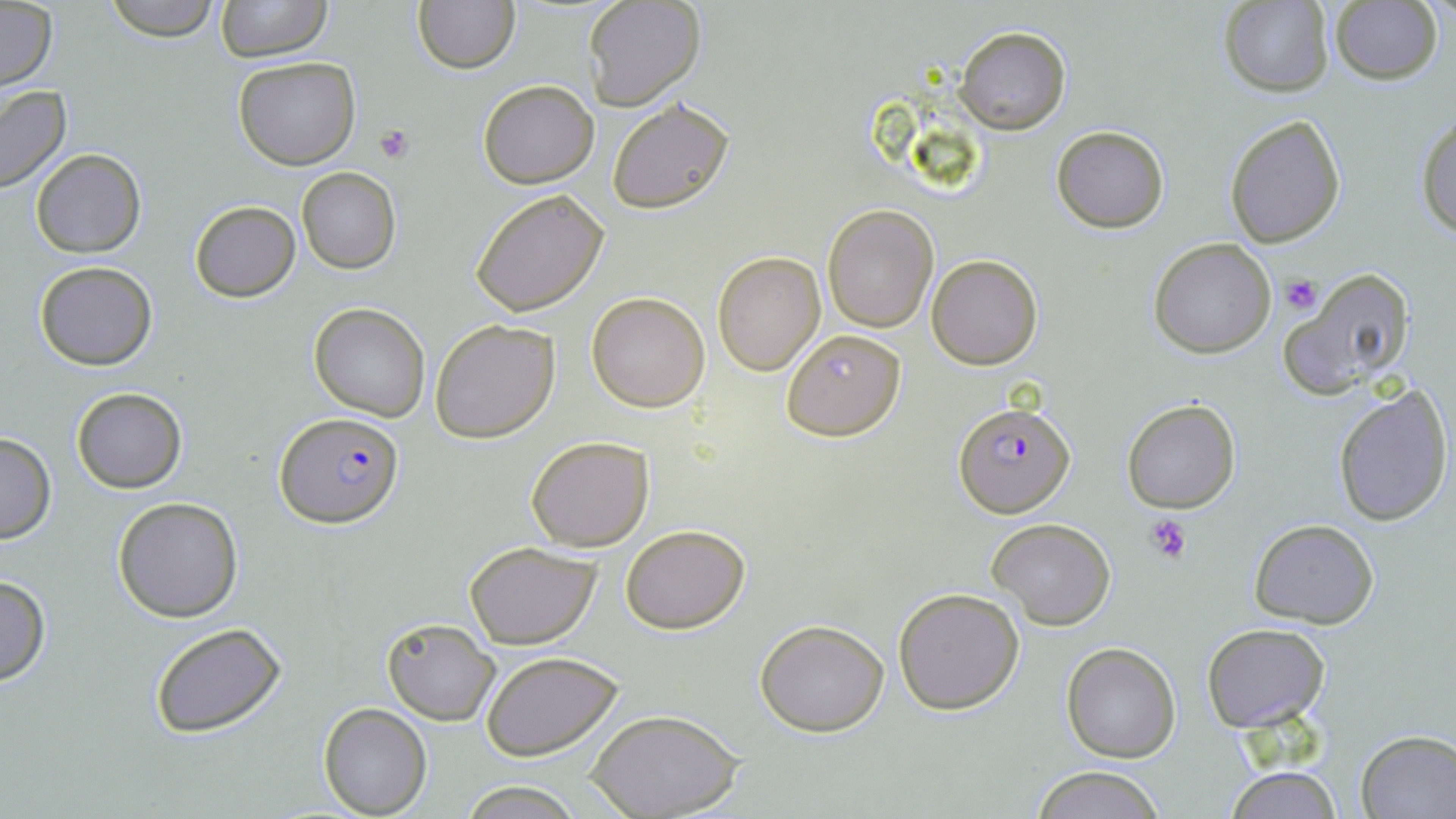
Approximate bounding boxes as named x1/y1/x2/y2 corners in pixels. Plasmodium falciparum-infected red blood cell locations: (x1=953, y1=401, x2=1074, y2=515), (x1=276, y1=411, x2=405, y2=527). Uninfected red blood cell locations: (x1=101, y1=0, x2=223, y2=42), (x1=216, y1=0, x2=332, y2=62), (x1=1217, y1=0, x2=1335, y2=96), (x1=413, y1=1, x2=520, y2=73), (x1=582, y1=1, x2=705, y2=110), (x1=1331, y1=2, x2=1444, y2=84), (x1=0, y1=3, x2=56, y2=91), (x1=955, y1=25, x2=1070, y2=134), (x1=234, y1=55, x2=360, y2=169), (x1=478, y1=79, x2=599, y2=188), (x1=0, y1=86, x2=72, y2=193), (x1=606, y1=96, x2=736, y2=214), (x1=1224, y1=114, x2=1346, y2=247), (x1=1414, y1=114, x2=1456, y2=239), (x1=1051, y1=126, x2=1170, y2=233), (x1=31, y1=148, x2=146, y2=258), (x1=296, y1=167, x2=402, y2=275), (x1=470, y1=188, x2=610, y2=317), (x1=189, y1=201, x2=300, y2=302), (x1=823, y1=205, x2=939, y2=333), (x1=1148, y1=238, x2=1277, y2=357), (x1=712, y1=251, x2=826, y2=376), (x1=928, y1=254, x2=1043, y2=370), (x1=33, y1=261, x2=158, y2=370), (x1=1281, y1=269, x2=1416, y2=401), (x1=587, y1=291, x2=710, y2=411), (x1=309, y1=302, x2=431, y2=422), (x1=430, y1=319, x2=560, y2=442), (x1=782, y1=329, x2=905, y2=440), (x1=1331, y1=383, x2=1454, y2=527), (x1=70, y1=387, x2=189, y2=493), (x1=1120, y1=398, x2=1242, y2=514), (x1=0, y1=432, x2=55, y2=545), (x1=525, y1=434, x2=655, y2=552), (x1=112, y1=496, x2=245, y2=623), (x1=986, y1=518, x2=1116, y2=631), (x1=1248, y1=518, x2=1379, y2=628), (x1=619, y1=524, x2=750, y2=633), (x1=464, y1=541, x2=602, y2=649), (x1=0, y1=574, x2=50, y2=686), (x1=893, y1=588, x2=1024, y2=714), (x1=381, y1=616, x2=502, y2=726), (x1=754, y1=618, x2=891, y2=736), (x1=149, y1=621, x2=287, y2=738), (x1=1200, y1=621, x2=1329, y2=732), (x1=1062, y1=642, x2=1181, y2=764), (x1=479, y1=650, x2=626, y2=761), (x1=318, y1=703, x2=431, y2=817), (x1=589, y1=709, x2=741, y2=818), (x1=1355, y1=729, x2=1456, y2=817), (x1=1029, y1=765, x2=1166, y2=819), (x1=1223, y1=765, x2=1345, y2=819), (x1=458, y1=781, x2=582, y2=817). Platelet locations: (x1=374, y1=123, x2=416, y2=163), (x1=1281, y1=276, x2=1320, y2=313), (x1=1145, y1=513, x2=1191, y2=563). Slide-level diagnosis: Plasmodium falciparum. Thin blood film. One field of a larger specimen. Captured at 1000x magnification. Light microscopy. Image is 1456×819 pixels. May-Grünwald-Giemsa-stained preparation.